Report the malaria status of this cell.
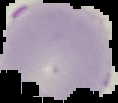
It is uninfected.

Summary:
  - Image size: 118×103 pixels
  - Image type: cell region segmented out of the field of view; surrounding area masked to black
  - Preparation: thin blood smear